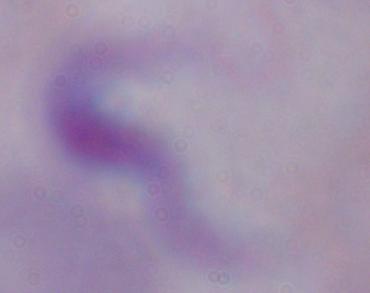
modality = photomicrograph
magnification = 1000x
identification = trypanosome